State the blood parasite species.
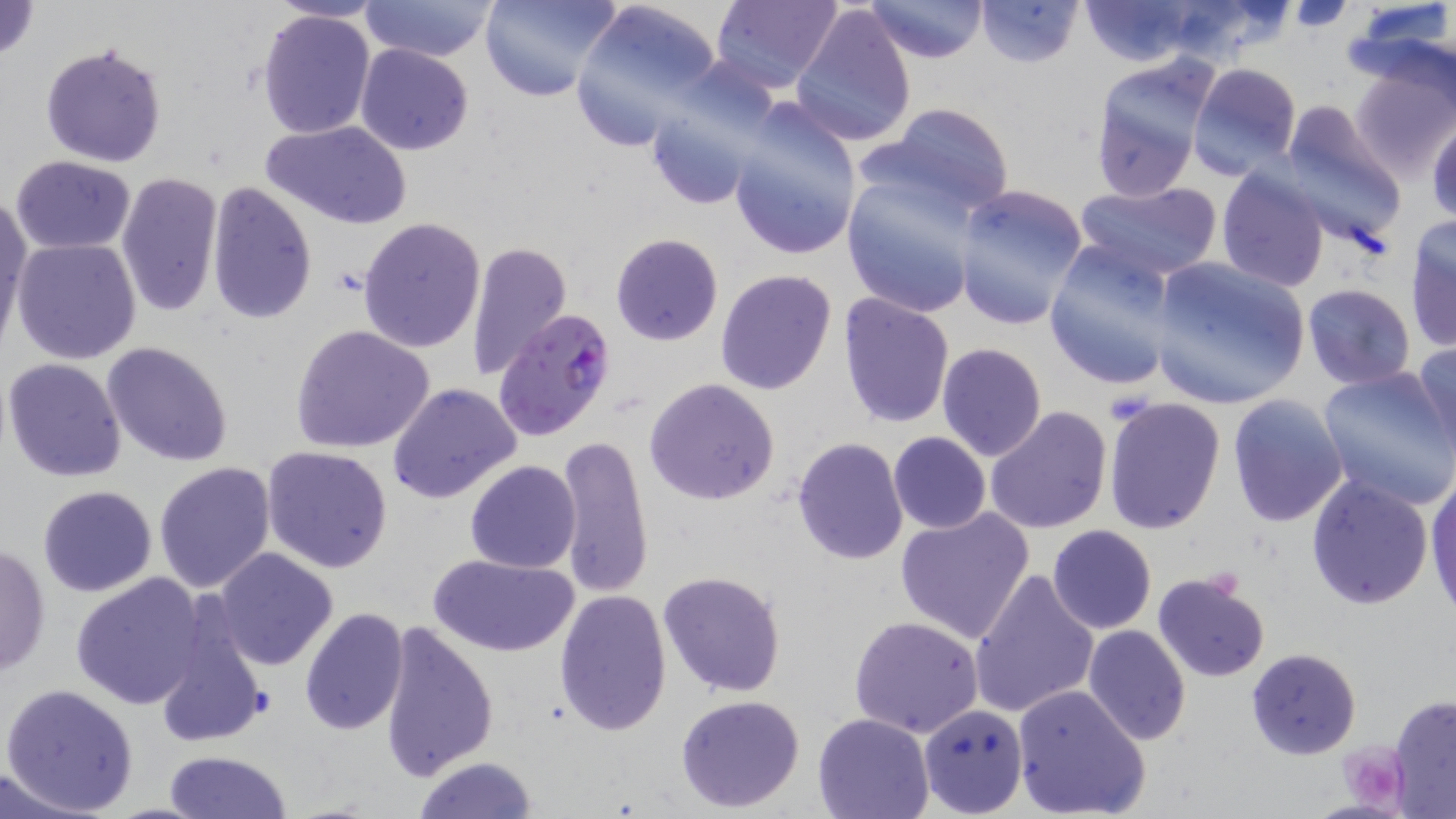

Plasmodium falciparum.

Summary:
  - Coordinate format: approximate bounding boxes as (x1, y1, x2, y2) in pixels
  - Plasmodium falciparum-infected red blood cell locations: (491, 307, 619, 443)
  - Uninfected red blood cell locations: (0, 0, 41, 64), (358, 0, 500, 65), (479, 0, 623, 104), (569, 0, 726, 151), (710, 0, 843, 93), (862, 0, 988, 65), (974, 0, 1085, 69), (1074, 0, 1205, 66), (789, 2, 918, 148), (1346, 2, 1455, 105), (256, 9, 376, 140), (40, 40, 169, 168), (355, 43, 474, 156), (1350, 59, 1455, 182), (1189, 62, 1303, 178), (1088, 66, 1214, 200), (642, 86, 774, 212), (724, 101, 863, 262), (1276, 102, 1408, 248), (869, 103, 1018, 223), (1428, 116, 1456, 224), (262, 119, 413, 231), (10, 154, 139, 254), (841, 166, 988, 317), (1215, 167, 1329, 292), (115, 173, 223, 317), (1075, 179, 1223, 282), (206, 181, 318, 324), (951, 186, 1092, 331), (0, 193, 31, 345), (357, 217, 486, 353), (1406, 219, 1456, 352), (611, 233, 723, 345), (11, 237, 142, 364), (1043, 240, 1184, 392), (466, 241, 573, 381), (1149, 255, 1311, 410), (714, 269, 838, 395), (1302, 284, 1416, 390), (838, 293, 956, 430), (290, 323, 438, 455), (1412, 339, 1456, 461), (102, 341, 234, 466), (936, 342, 1048, 461), (3, 357, 128, 482), (1315, 367, 1456, 511), (645, 377, 780, 504), (387, 382, 522, 504), (1226, 394, 1348, 527), (1102, 396, 1227, 535), (984, 406, 1112, 535), (887, 432, 991, 534), (555, 434, 654, 598), (791, 437, 908, 565), (261, 446, 394, 574), (464, 460, 582, 572), (151, 461, 277, 595), (1426, 469, 1456, 619), (1304, 473, 1435, 610), (37, 485, 158, 597), (894, 507, 1035, 643), (1047, 525, 1157, 634), (0, 542, 52, 679), (211, 547, 339, 672), (427, 552, 579, 658), (969, 566, 1099, 720), (656, 569, 786, 698), (72, 572, 207, 708), (1152, 572, 1271, 682), (554, 588, 671, 734), (299, 608, 409, 735), (153, 609, 265, 749), (848, 615, 986, 738), (376, 621, 500, 781), (1082, 626, 1191, 746), (1245, 648, 1363, 760), (1, 682, 140, 815), (1010, 683, 1151, 819), (675, 693, 806, 811), (1388, 694, 1456, 817), (918, 702, 1029, 817), (811, 713, 935, 819), (164, 749, 291, 818), (411, 756, 540, 818), (0, 769, 103, 819)
  - Platelet locations: (1341, 741, 1402, 808)
  - Preparation: thin blood smear
  - Magnification: 1000x
  - Modality: optical microscopy
  - Stain: May-Grünwald-Giemsa
  - Field of view: single
  - Image size: 1456×819 pixels